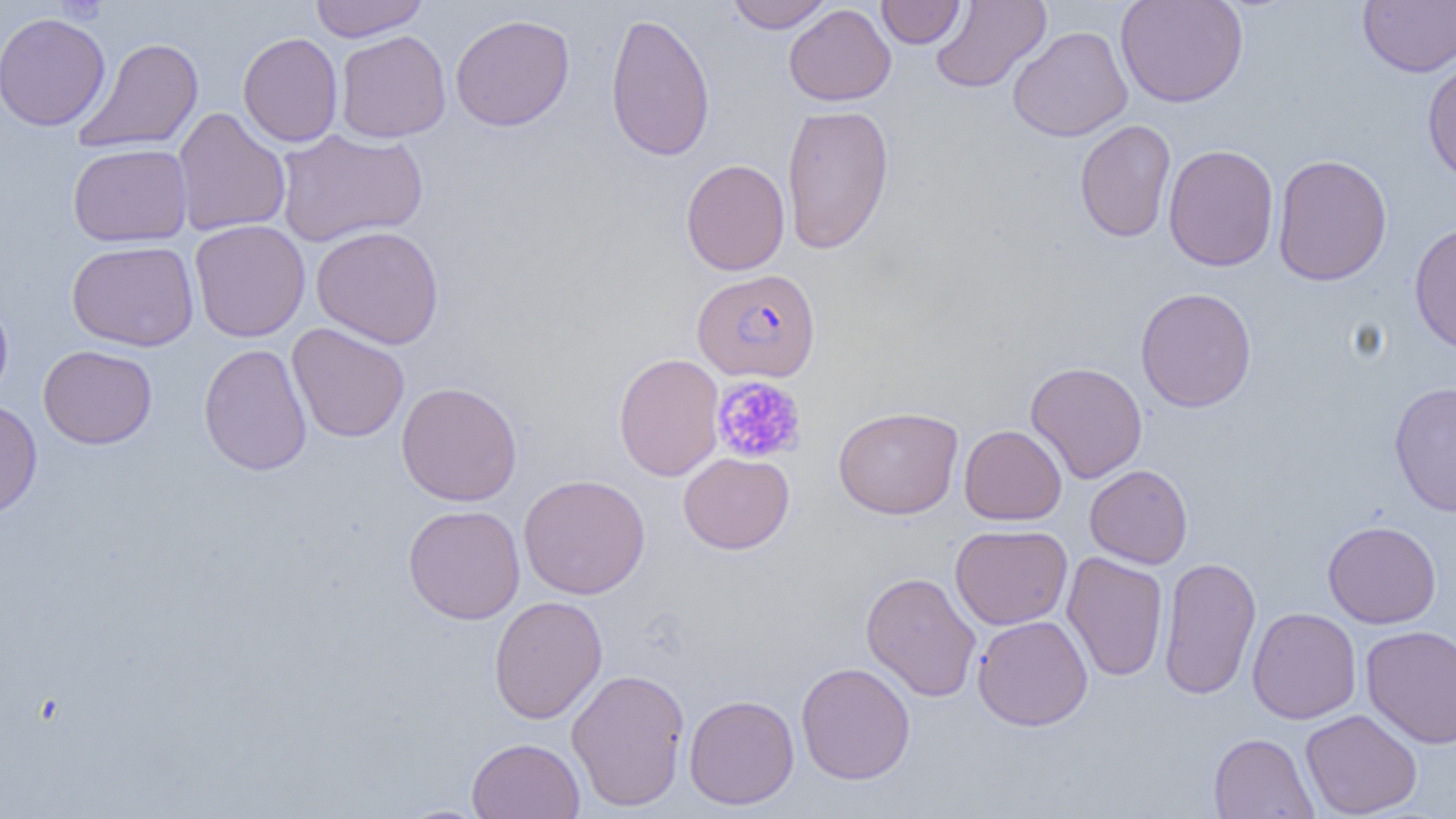

Summary:
  - Coordinate format: approximate bounding boxes as named x1/y1/x2/y2 corners in pixels
  - Uninfected red blood cell locations: (x1=309, y1=0, x2=430, y2=42), (x1=724, y1=0, x2=835, y2=33), (x1=929, y1=0, x2=1051, y2=93), (x1=1115, y1=0, x2=1249, y2=108), (x1=1358, y1=0, x2=1456, y2=77), (x1=876, y1=1, x2=965, y2=48), (x1=784, y1=3, x2=896, y2=106), (x1=604, y1=11, x2=715, y2=162), (x1=0, y1=12, x2=111, y2=132), (x1=450, y1=14, x2=575, y2=131), (x1=1008, y1=26, x2=1133, y2=142), (x1=335, y1=30, x2=451, y2=143), (x1=238, y1=31, x2=343, y2=147), (x1=73, y1=37, x2=204, y2=154), (x1=1421, y1=55, x2=1456, y2=185), (x1=781, y1=104, x2=895, y2=254), (x1=172, y1=107, x2=291, y2=237), (x1=1074, y1=119, x2=1176, y2=243), (x1=275, y1=128, x2=428, y2=248), (x1=67, y1=143, x2=193, y2=246), (x1=1163, y1=144, x2=1279, y2=272), (x1=1272, y1=153, x2=1392, y2=286), (x1=680, y1=158, x2=790, y2=275), (x1=189, y1=220, x2=311, y2=342), (x1=1408, y1=221, x2=1456, y2=355), (x1=311, y1=225, x2=445, y2=349), (x1=67, y1=240, x2=199, y2=352), (x1=1135, y1=287, x2=1257, y2=413), (x1=0, y1=292, x2=13, y2=405), (x1=287, y1=323, x2=410, y2=443), (x1=198, y1=343, x2=313, y2=476), (x1=38, y1=344, x2=157, y2=449), (x1=613, y1=352, x2=724, y2=482), (x1=1025, y1=361, x2=1148, y2=484), (x1=1389, y1=381, x2=1456, y2=517), (x1=396, y1=382, x2=523, y2=506), (x1=0, y1=399, x2=42, y2=519), (x1=833, y1=406, x2=963, y2=519), (x1=959, y1=425, x2=1067, y2=525), (x1=679, y1=452, x2=794, y2=554), (x1=1084, y1=465, x2=1193, y2=568), (x1=518, y1=474, x2=650, y2=599), (x1=403, y1=504, x2=526, y2=624), (x1=1323, y1=520, x2=1441, y2=628), (x1=950, y1=524, x2=1073, y2=629), (x1=1062, y1=551, x2=1168, y2=683), (x1=1158, y1=555, x2=1261, y2=700), (x1=861, y1=572, x2=981, y2=702), (x1=489, y1=595, x2=607, y2=724), (x1=1247, y1=607, x2=1361, y2=724), (x1=972, y1=615, x2=1093, y2=731), (x1=1360, y1=624, x2=1456, y2=749), (x1=795, y1=661, x2=915, y2=784), (x1=566, y1=668, x2=690, y2=811), (x1=684, y1=694, x2=800, y2=809), (x1=1299, y1=709, x2=1423, y2=818), (x1=1208, y1=733, x2=1318, y2=819), (x1=466, y1=737, x2=585, y2=818), (x1=392, y1=803, x2=495, y2=818)
  - Plasmodium falciparum-infected red blood cell locations: (x1=691, y1=268, x2=821, y2=383)
  - Platelet locations: (x1=712, y1=375, x2=807, y2=464)
  - Slide-level diagnosis: Plasmodium falciparum
  - Field of view: single
  - Magnification: 1000x
  - Preparation: thin blood smear
  - Image size: 1456×819 pixels
  - Modality: light microscopy